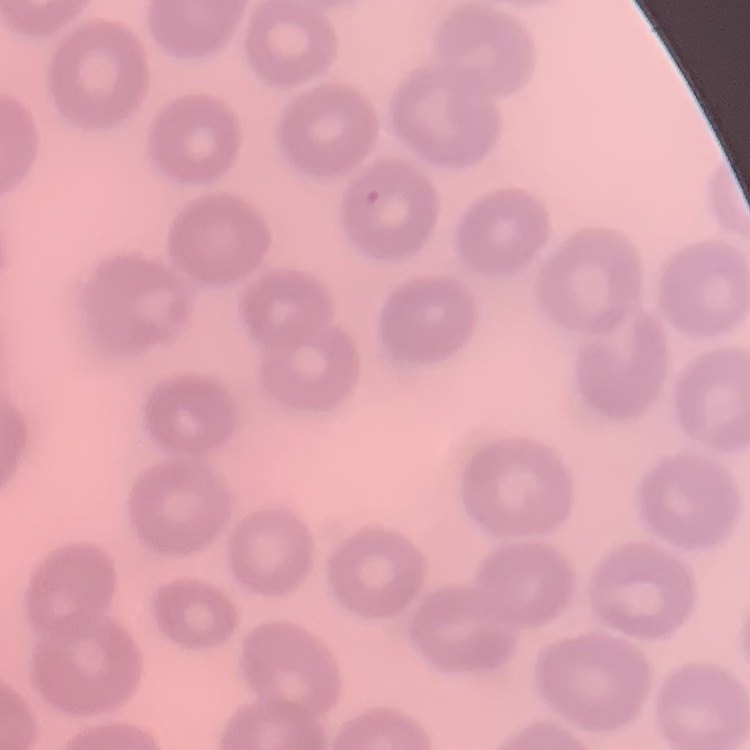

The red blood cells exhibit no rouleaux formation. One tile cut from a larger photomicrograph. Thin blood smear. Stained with either Field's or Giemsa.